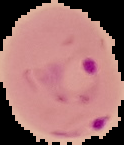

preparation = thin blood smear
malaria status = parasitized
image type = segmented cell region with the area outside set to black
image size = 124×145 pixels